Locate every parasitized RBC.
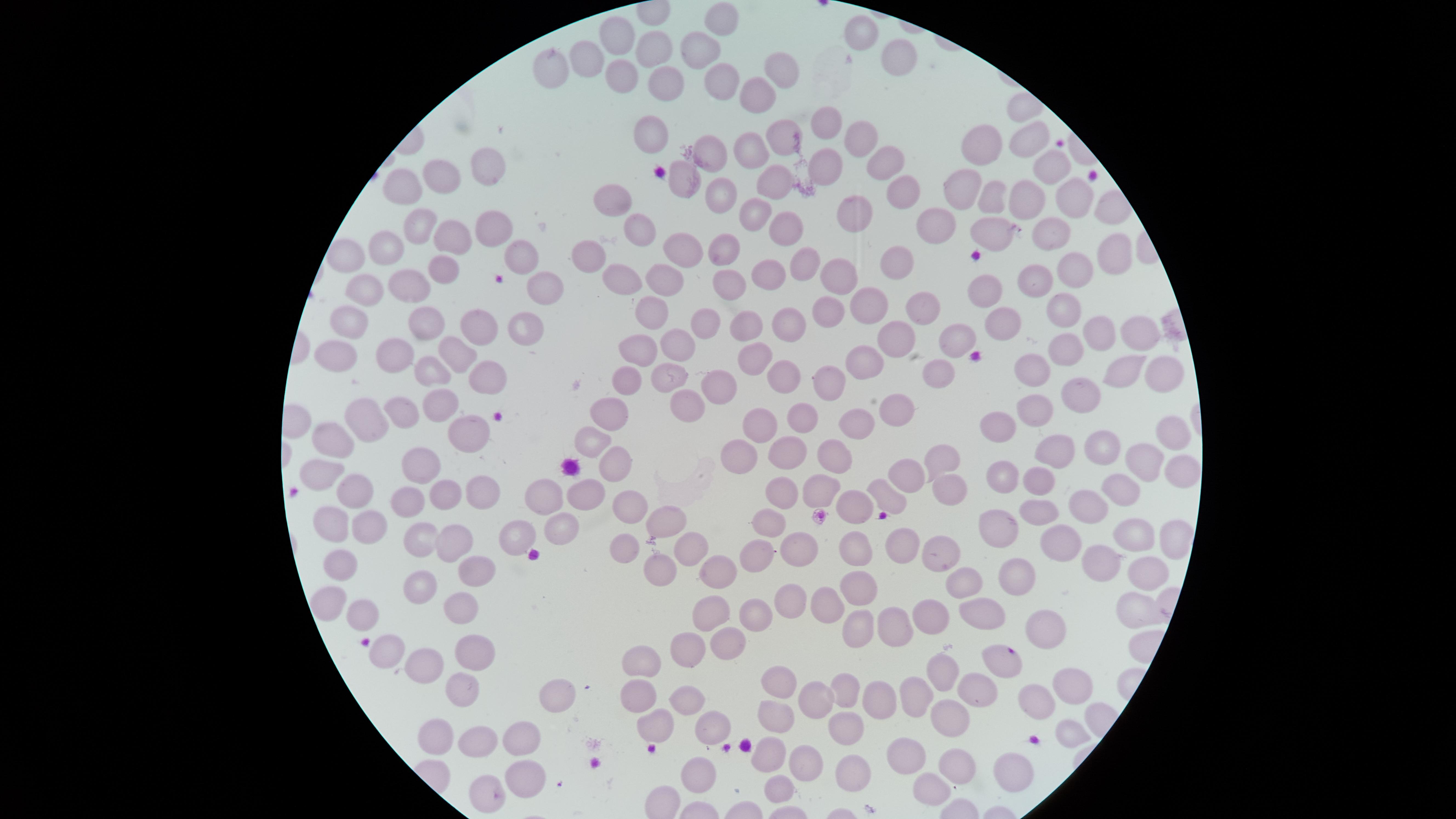

No parasitized RBCs identified.

{
  "image_size": "1456×819 pixels",
  "uninfected_RBCs": "approximate marker points as (x, y) in pixels: (725, 19), (866, 33), (618, 36), (699, 45), (656, 51), (593, 52), (901, 56), (554, 61), (784, 71), (625, 74), (714, 74), (659, 76), (762, 92), (824, 125), (857, 132), (782, 134), (645, 136), (1031, 136), (980, 143), (748, 147), (716, 155), (881, 161), (492, 165), (828, 165), (1057, 167), (682, 173), (398, 181), (438, 181), (959, 182), (770, 183), (898, 186), (720, 192), (611, 195), (985, 195), (1076, 195), (1023, 200), (862, 206), (754, 209), (939, 216), (792, 218), (418, 219), (496, 221), (997, 227), (632, 231), (1061, 236), (448, 239), (386, 245), (678, 246), (587, 249), (719, 251), (349, 253), (806, 254), (1105, 255), (521, 256), (893, 262), (1078, 266), (439, 270), (840, 271), (616, 272), (671, 273), (1034, 276), (734, 278), (763, 279), (363, 280), (543, 281), (403, 286), (984, 289), (863, 304), (922, 306), (653, 308), (830, 309), (355, 311), (1060, 313), (709, 318), (786, 319), (421, 320), (745, 321), (996, 324), (476, 327), (518, 327), (1102, 329), (1139, 329), (894, 338), (949, 340), (672, 344), (336, 345), (638, 347), (1076, 350), (389, 351), (455, 351), (755, 358), (1039, 360), (863, 362), (1124, 363), (784, 365), (486, 367), (429, 372), (934, 372), (1161, 372), (632, 376), (667, 376), (828, 379), (709, 393), (1074, 393), (686, 402), (433, 405), (893, 405), (1033, 405), (611, 409), (402, 410), (372, 413), (808, 414), (850, 418), (763, 420), (999, 420), (1169, 431), (461, 432), (337, 433), (592, 433), (1100, 446), (741, 449), (1046, 449), (786, 450), (832, 451), (1138, 455), (943, 461), (609, 462), (413, 464), (1177, 464), (327, 469), (916, 469), (1003, 471), (1041, 477), (1118, 483), (588, 484), (816, 484), (946, 484), (776, 487), (482, 490), (540, 490), (456, 492), (883, 492), (355, 494), (861, 498), (419, 501), (1097, 501), (629, 508), (1037, 510), (670, 516), (774, 524), (1000, 526), (559, 527), (333, 528), (366, 530), (1138, 532), (524, 534), (1061, 538), (1169, 539), (455, 540), (418, 542), (809, 544), (694, 545), (623, 546), (851, 547), (901, 547), (760, 550), (945, 552), (477, 565), (1105, 566), (663, 567), (725, 567), (346, 569), (1007, 577), (1137, 578), (859, 582), (966, 583), (415, 593), (330, 598), (983, 602), (824, 604), (464, 607), (711, 608), (360, 609), (928, 609), (799, 610), (1125, 610), (754, 612), (853, 618), (891, 623), (1042, 631), (724, 644), (689, 649), (377, 652), (475, 654), (1000, 661), (648, 662), (422, 663), (942, 671), (775, 681), (1058, 686), (465, 688), (843, 690), (916, 690), (971, 692), (640, 694), (687, 694), (817, 697), (876, 702), (1029, 702), (550, 704), (786, 709), (656, 716), (954, 719), (711, 723), (444, 727), (846, 729), (524, 740), (478, 743), (915, 753), (772, 754), (960, 760), (808, 761), (1011, 765), (854, 767), (522, 775), (706, 777), (781, 786), (929, 788), (486, 795)",
  "preparation": "thin blood film",
  "field_of_view": "single",
  "visible_region": "circular",
  "stain": "Giemsa",
  "capture": "smartphone photograph through the microscope eyepiece"
}